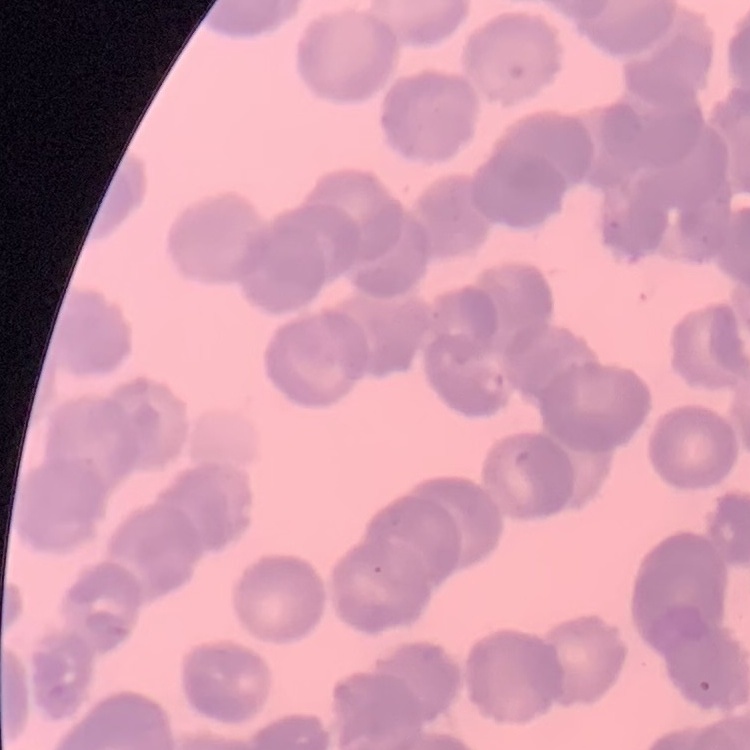 The red blood cells show rouleaux formation. Field's or Giemsa stain. Thin blood film. One tile cut from a larger photomicrograph.